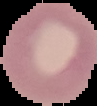

image_size: 97×106 pixels
malaria_status: uninfected
image_type: segmented cell region with the area outside set to black
preparation: thin blood film